Locate and identify every blood parasite.
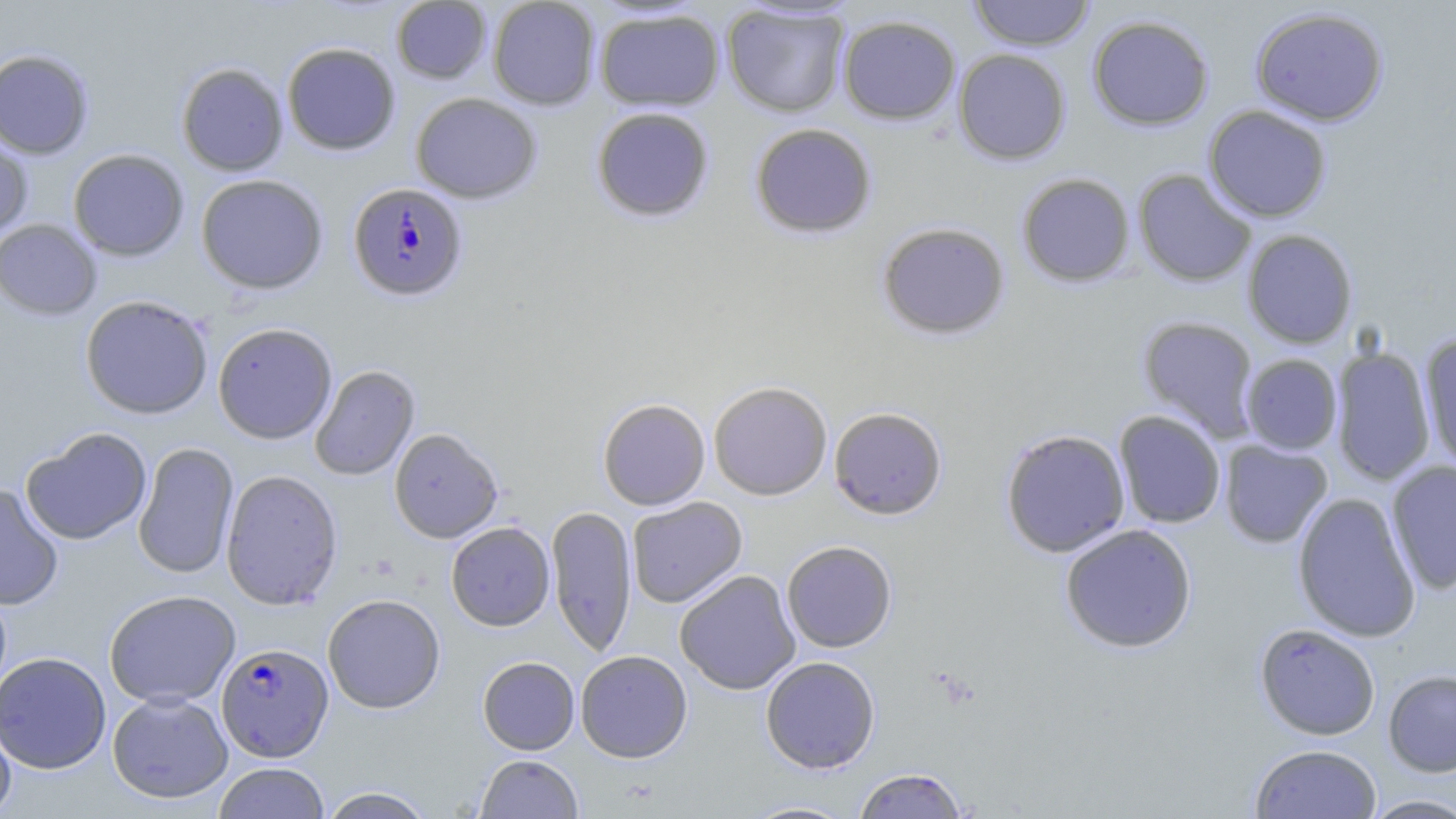
Approximate bounding boxes as (x1, y1, x2, y2) in pixels.
Plasmodium falciparum-infected red blood cells: (348, 182, 468, 301), (216, 642, 334, 761).
No Plasmodium ovale, Plasmodium malariae, Plasmodium vivax, Babesia divergens, or Trypanosoma brucei observed.

slide-level diagnosis = Plasmodium falciparum
uninfected red blood cell locations = approximate bounding boxes as (x1, y1, x2, y2) in pixels: (487, 0, 601, 110), (967, 0, 1095, 51), (390, 1, 492, 84), (721, 3, 851, 117), (1250, 6, 1389, 126), (594, 7, 725, 112), (837, 14, 961, 125), (1087, 14, 1214, 131), (282, 42, 401, 155), (953, 48, 1071, 165), (0, 49, 95, 160), (176, 62, 289, 176), (410, 92, 542, 204), (1203, 105, 1332, 223), (591, 106, 714, 222), (749, 122, 877, 239), (0, 131, 33, 239), (68, 149, 189, 261), (1132, 169, 1257, 288), (1016, 172, 1136, 287), (196, 173, 329, 294), (0, 219, 102, 320), (876, 221, 1010, 339), (1242, 229, 1358, 349), (80, 295, 214, 419), (1137, 315, 1261, 442), (213, 322, 338, 444), (1418, 333, 1456, 472), (1330, 345, 1436, 486), (1241, 354, 1343, 455), (309, 364, 420, 481), (708, 380, 832, 500), (597, 398, 710, 510), (829, 406, 947, 519), (1113, 410, 1227, 528), (21, 427, 153, 545), (389, 428, 504, 543), (1000, 428, 1130, 557), (1219, 440, 1333, 548), (133, 442, 239, 579), (1386, 460, 1456, 594), (220, 468, 343, 610), (0, 485, 64, 611), (1292, 491, 1421, 643), (626, 496, 747, 608), (546, 504, 637, 657), (446, 521, 555, 631), (1059, 523, 1197, 653), (781, 540, 897, 652), (674, 570, 801, 695), (104, 590, 241, 708), (322, 593, 446, 714), (1253, 623, 1381, 740), (575, 650, 692, 762), (0, 651, 111, 774), (478, 656, 580, 755), (760, 656, 880, 773), (1383, 670, 1456, 776), (107, 691, 233, 803), (0, 714, 17, 819), (1249, 744, 1382, 818), (475, 754, 583, 819), (213, 762, 330, 819), (854, 768, 968, 818), (318, 786, 437, 818), (1360, 794, 1456, 818), (741, 800, 860, 818)
field of view = single
magnification = 1000x
preparation = thin blood film
modality = light microscopy
image size = 1456×819 pixels
stain = May-Grünwald-Giemsa